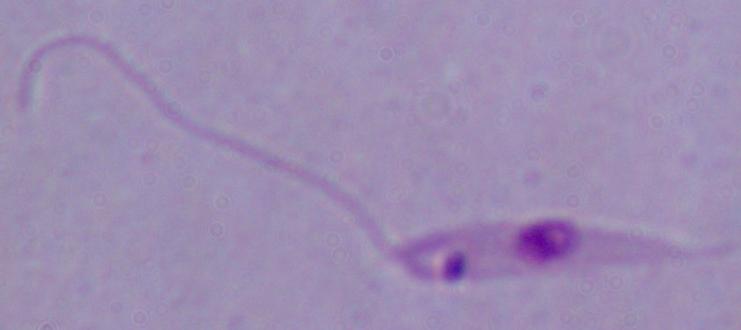
Summary:
  - Modality: micrograph
  - Identification: Leishmania
  - Magnification: 1000x